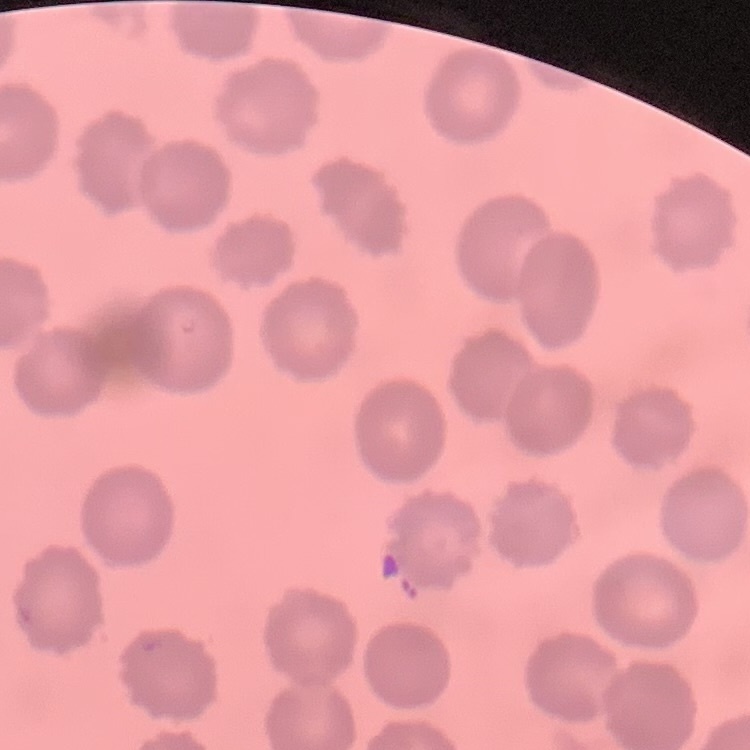
Summary:
  - Erythrocyte morphology: no rouleaux formation
  - Preparation: thin blood smear
  - Image type: square crop of a larger photomicrograph
  - Stain: Field's or Giemsa